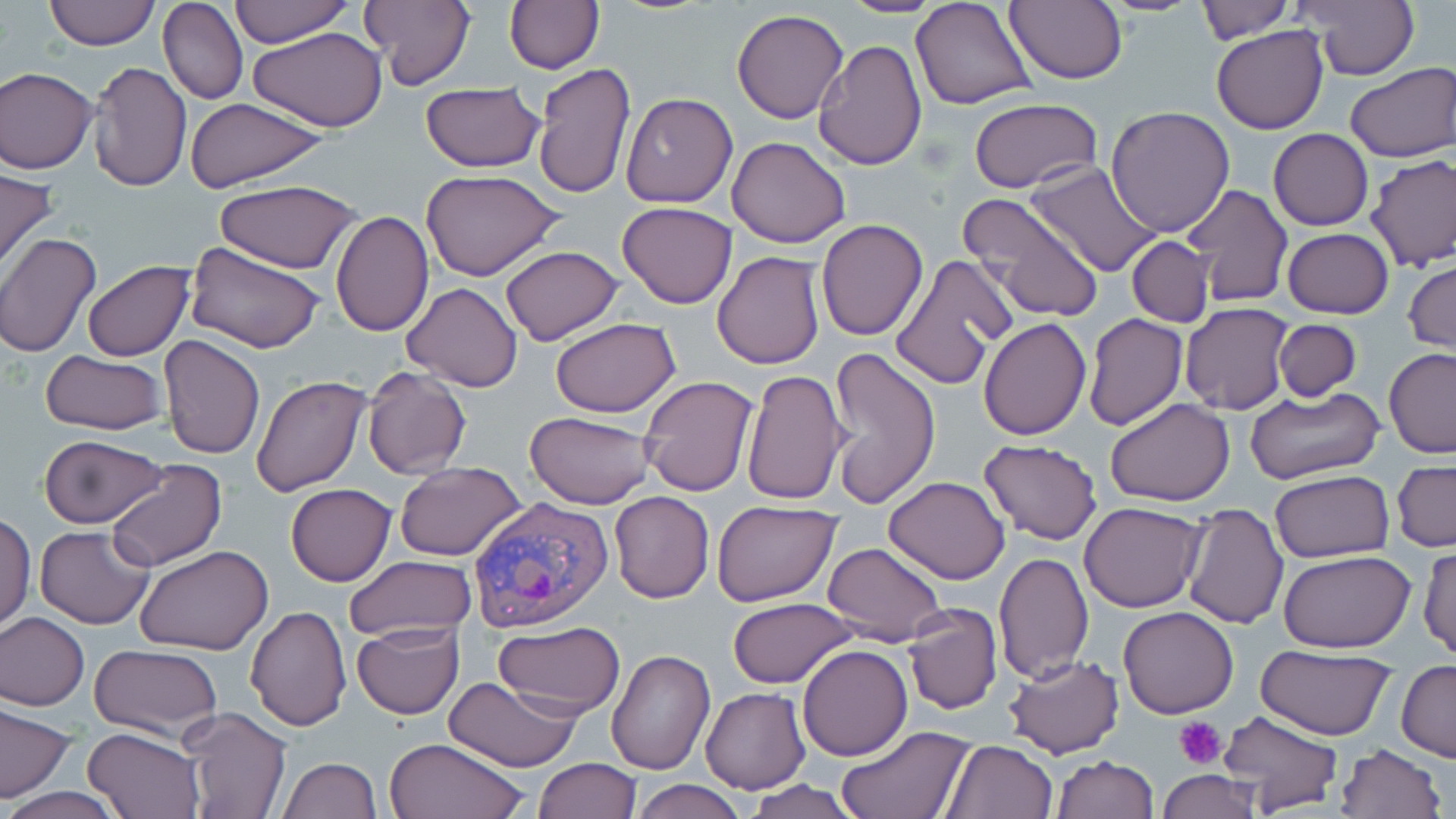

Approximate bounding boxes as (x1,y1)-(x2,y2) corner pairs in pixels. Platelet locations: (1174,717)-(1226,768). Uninfected red blood cell locations: (43,0)-(161,50), (158,0)-(248,105), (230,0)-(355,45), (359,0)-(476,89), (503,0)-(605,74), (836,0)-(947,17), (910,0)-(1037,112), (1006,0)-(1127,84), (1194,0)-(1293,44), (1297,0)-(1417,83), (732,9)-(849,124), (1210,25)-(1329,134), (248,27)-(389,129), (812,37)-(926,172), (88,61)-(192,193), (533,62)-(635,199), (1344,63)-(1454,164), (0,66)-(98,173), (418,81)-(546,173), (620,92)-(737,208), (183,97)-(334,192), (969,99)-(1101,195), (1106,105)-(1235,236), (1269,129)-(1374,230), (727,136)-(851,247), (1365,153)-(1456,272), (1025,161)-(1163,278), (0,165)-(58,274), (419,170)-(568,281), (213,180)-(364,270), (1182,184)-(1294,307), (956,192)-(1105,326), (617,201)-(739,309), (330,209)-(434,337), (816,219)-(928,341), (1282,227)-(1395,319), (0,234)-(100,356), (1127,237)-(1212,327), (718,239)-(921,358), (184,240)-(326,354), (501,247)-(622,346), (712,251)-(826,369), (888,253)-(1017,390), (1405,257)-(1455,356), (82,260)-(194,361), (403,283)-(523,392), (1179,304)-(1293,416), (1083,314)-(1188,432), (977,316)-(1092,440), (549,318)-(680,418), (1274,319)-(1361,401), (159,335)-(265,459), (826,345)-(943,508), (1383,348)-(1456,457), (40,350)-(166,435), (361,367)-(472,479), (740,367)-(848,508), (251,374)-(372,496), (638,375)-(759,497), (1245,386)-(1383,486), (1104,396)-(1236,506), (524,412)-(656,508), (39,434)-(168,529), (978,438)-(1102,545), (104,460)-(227,572), (1392,460)-(1455,552), (393,461)-(525,562), (1269,471)-(1395,564), (885,476)-(1009,585), (285,483)-(396,586), (609,491)-(715,603), (710,499)-(840,604), (1080,501)-(1207,611), (1181,502)-(1288,629), (0,511)-(35,632), (35,527)-(154,628), (821,540)-(948,645), (134,544)-(275,655), (1418,545)-(1455,661), (992,550)-(1094,682), (1278,550)-(1417,653), (343,553)-(477,642), (727,598)-(857,688), (903,602)-(1003,715), (1117,605)-(1239,718), (245,607)-(351,730), (0,613)-(90,709), (494,620)-(624,714), (352,621)-(465,719), (89,644)-(223,739), (797,644)-(912,760), (606,646)-(715,776), (1255,648)-(1396,741), (1002,653)-(1126,759), (1397,664)-(1456,762), (444,677)-(582,771), (701,688)-(811,794), (0,706)-(75,802), (178,708)-(291,819), (1217,709)-(1342,815), (835,723)-(971,817), (83,726)-(207,818), (384,736)-(530,819), (943,738)-(1059,819), (1334,742)-(1447,819), (1052,754)-(1159,818), (278,757)-(381,818), (534,758)-(639,818), (1157,771)-(1262,817), (631,779)-(748,818), (740,780)-(864,818), (5,786)-(119,819). Plasmodium vivax-infected red blood cell locations: (465,496)-(614,634). Slide-level diagnosis: Plasmodium vivax. Light microscopy. Single field of view. Captured at 1000x magnification. May-Grünwald-Giemsa-stained preparation. Thin blood smear. Image is 1456×819 pixels.